Locate every malaria parasite.
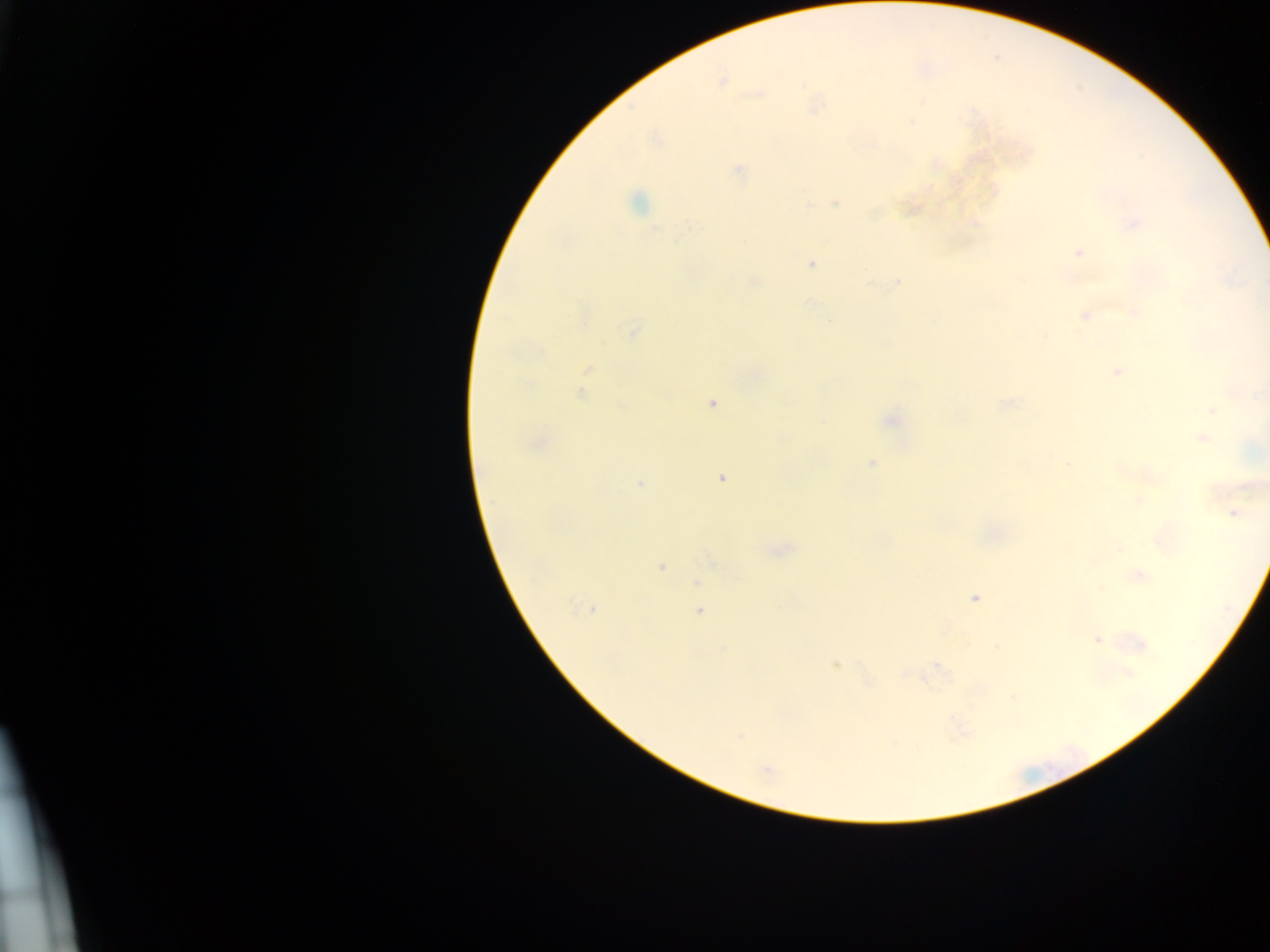
Approximate centers as [x, y] in pixels.
Malaria parasites: [723, 81], [912, 121], [738, 169], [637, 203], [836, 203], [808, 205], [1135, 224], [692, 225], [1079, 252], [812, 263], [753, 282], [897, 283], [1135, 313], [1084, 316], [632, 331], [588, 369], [1117, 371], [582, 394], [712, 403], [1008, 404], [621, 405], [1211, 410], [891, 421], [1202, 438], [872, 462], [721, 478], [639, 484], [1249, 485], [1139, 500], [1234, 513], [1119, 548], [661, 566], [1139, 576], [697, 582], [1101, 589], [975, 597], [588, 609], [699, 612], [1097, 639], [835, 665], [1128, 673], [870, 682], [740, 737], [767, 770].

preparation = thick blood film
capture = mobile-phone photograph through a microscope
field of view = single
image size = 1270×952 pixels
country = Ghana